Report the malaria status of this cell.
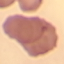
Uninfected.

Summary:
  - Capture: smartphone camera at the microscope eyepiece
  - Stain: Giemsa
  - Preparation: thin smear
  - Image type: automatically extracted cell patch, resized to 64 × 64 pixels